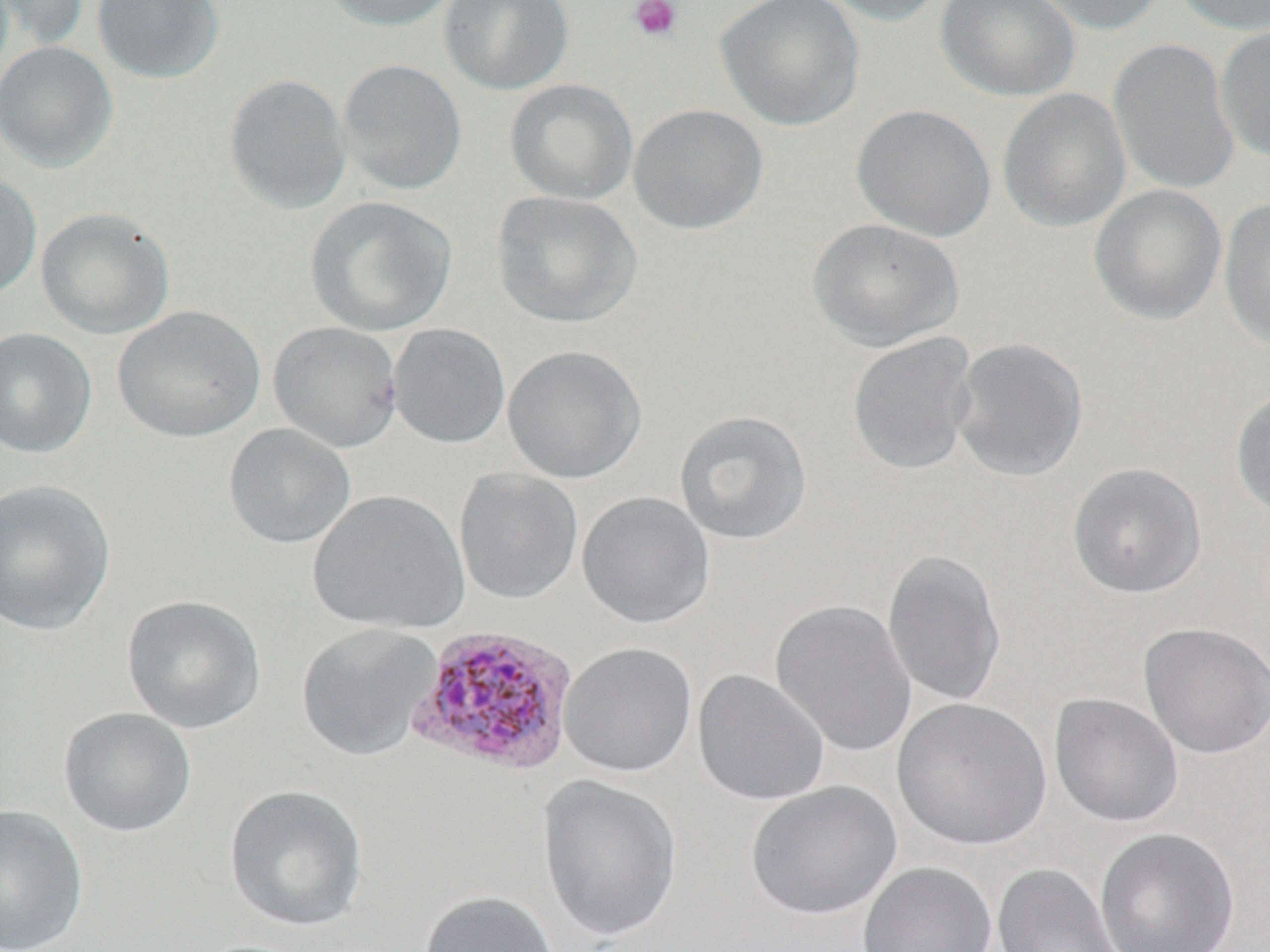
Approximate bounding boxes as (x1,y1)-(x2,y2) corner pairs in pixels. Platelet locations: (628,0)-(683,42). Plasmodium vivax-infected red blood cell locations: (408,624)-(580,775). Uninfected red blood cell locations: (1,0)-(89,50), (92,0)-(225,83), (320,0)-(459,32), (438,0)-(575,95), (714,0)-(865,131), (816,0)-(946,26), (935,0)-(1081,101), (1026,0)-(1168,36), (1173,0)-(1270,35), (1215,24)-(1270,164), (1108,38)-(1240,196), (0,40)-(119,173), (337,59)-(468,195), (223,73)-(352,215), (504,78)-(638,205), (998,88)-(1131,233), (628,103)-(768,234), (852,104)-(997,241), (0,170)-(42,301), (1089,184)-(1226,325), (491,191)-(642,329), (304,196)-(457,337), (1219,196)-(1270,352), (35,206)-(175,339), (807,217)-(964,350), (112,305)-(266,443), (268,321)-(403,452), (388,324)-(510,449), (0,327)-(97,459), (847,332)-(979,475), (950,336)-(1089,482), (502,344)-(647,484), (1231,387)-(1270,521), (673,410)-(812,546), (223,423)-(356,550), (1067,463)-(1207,599), (454,467)-(584,604), (0,479)-(116,636), (307,489)-(470,635), (577,491)-(715,630), (882,547)-(1006,708), (121,594)-(267,733), (771,599)-(917,757), (296,622)-(442,762), (1138,622)-(1270,759), (559,642)-(697,778), (693,669)-(830,806), (1049,692)-(1183,827), (892,697)-(1053,850), (59,707)-(197,837), (537,774)-(682,944), (746,780)-(902,920), (224,784)-(369,933), (1,802)-(89,952), (1095,827)-(1241,952), (857,861)-(997,952), (992,862)-(1126,952), (418,890)-(561,952). Slide-level diagnosis: Plasmodium vivax. Light microscopy. Image is 1270×952 pixels. Thin blood smear. May-Grünwald-Giemsa stain. 1000x magnification. Single field of view.